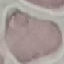
Malaria status: uninfected. Giemsa-stained preparation. Photographed with a smartphone camera at the microscope eyepiece. Thin smear of blood. Automatically extracted cell patch, resized to 64 × 64 pixels.